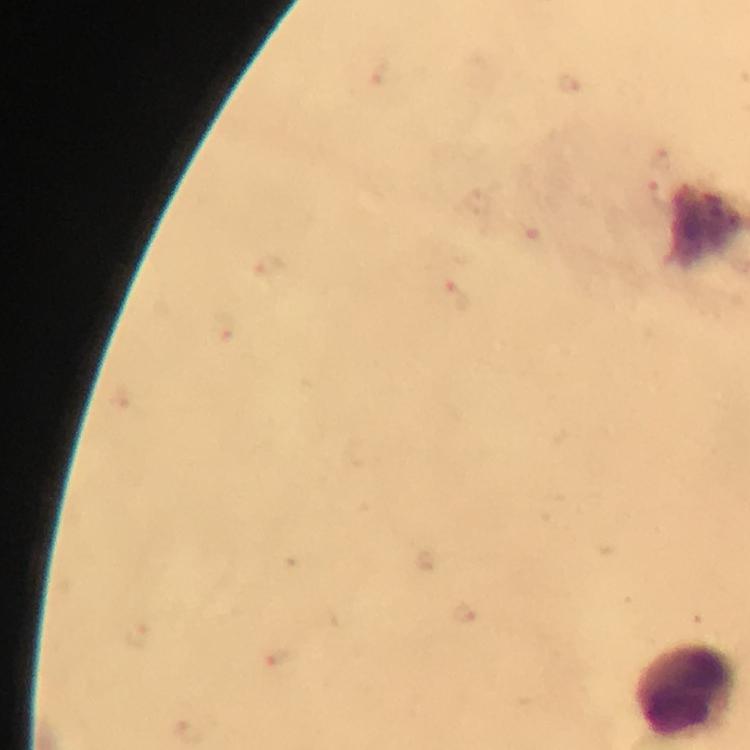 Approximate centers as {x, y} in pixels. Leukocyte locations: {684, 691}. Malaria parasite locations: {660, 196}, {268, 263}, {457, 297}, {224, 328}, {137, 634}, {280, 664}. Smartphone photograph taken through a microscope. From a malaria diagnostic workup. Immersion oil was used. Thick smear. At 100x magnification. Giemsa stain. Image is 750×750 pixels. Cropped region of a single field of view.